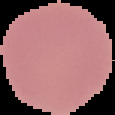
Malaria status: uninfected. From a thin blood film. Image is 115×115 pixels. Segmented cell region on a black background.